Classify this cell by malaria status.
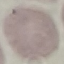
Uninfected.

Automatically extracted cell patch, resized to 64 × 64 pixels. Acquired by smartphone through the microscope eyepiece. Giemsa-stained preparation. Thin blood film.